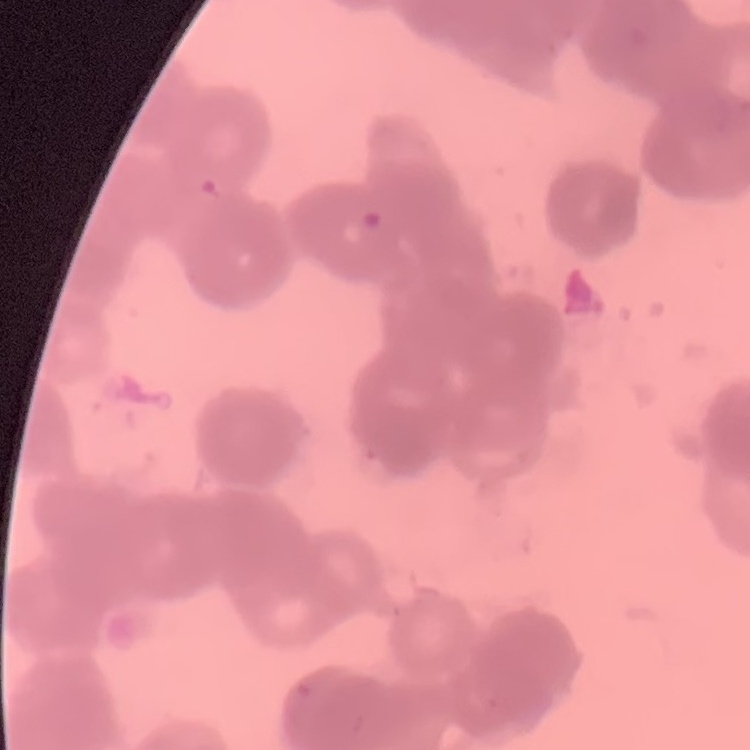

The erythrocytes exhibit rouleaux formation. Field's or Giemsa stain. Thin peripheral smear. One tile cut from a larger photomicrograph.